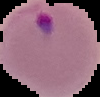
image_size: 100×97 pixels
preparation: thin blood smear
image_type: segmented cell region with the area outside set to black
result: malaria parasites detected